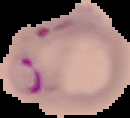 From a thin blood smear. Image is 130×118 pixels. Segmented cell region on a black background. Result: Plasmodium parasites detected.